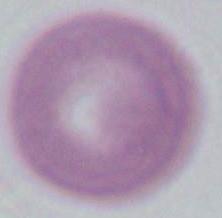

Summary:
  - Modality: micrograph
  - Identification: erythrocyte
  - Magnification: 1000x